Report the malaria status of this cell.
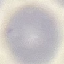
It is uninfected.

Summary:
  - Image type: cell patch, automatically extracted from a larger field of view and resized to 64 × 64 pixels
  - Capture: smartphone through the microscope eyepiece
  - Preparation: thin blood smear
  - Stain: Giemsa